Assess this cell for malaria.
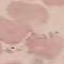
It is uninfected.

Summary:
  - Preparation: thin smear
  - Capture: smartphone through the microscope eyepiece
  - Stain: Giemsa
  - Image type: cell patch, automatically extracted from a larger field of view and resized to 64 × 64 pixels